Give the position of every leukocyte visible.
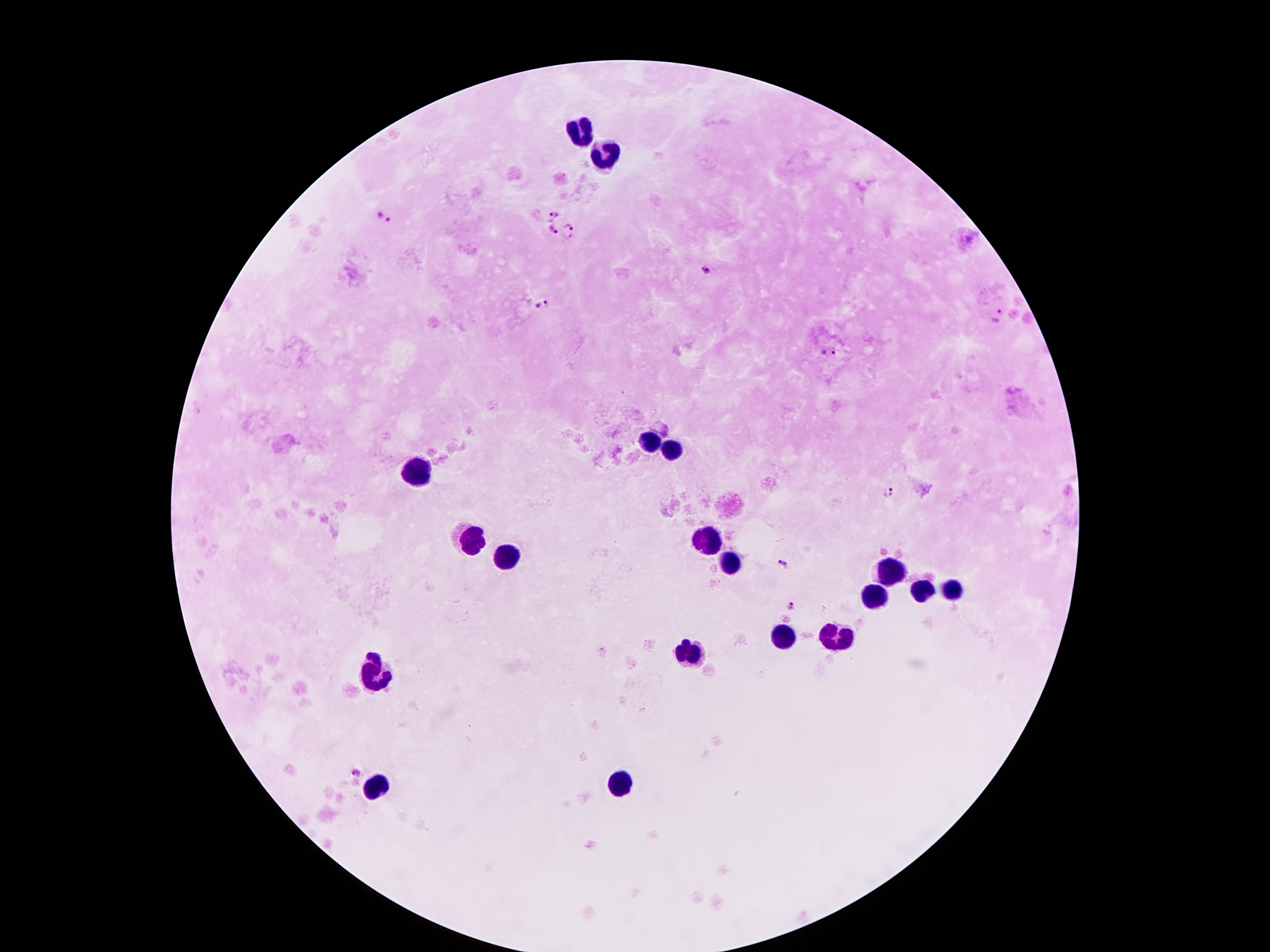
Approximate object centers, in pixels from the top-left corner.
Leukocytes: (x=584, y=133), (x=607, y=157), (x=651, y=440), (x=672, y=454), (x=418, y=475), (x=471, y=540), (x=706, y=540), (x=507, y=557), (x=729, y=566), (x=889, y=569), (x=924, y=592), (x=952, y=593), (x=874, y=599), (x=840, y=635), (x=782, y=637), (x=693, y=652), (x=376, y=675), (x=620, y=786), (x=377, y=790).

patient_malaria_status: infected with Plasmodium falciparum
preparation: thick peripheral-blood smear
field_of_view: one from this slide
malaria_parasite_locations: 'approximate object centers, in pixels from the top-left corner: (x=552, y=212), (x=384, y=218), (x=552, y=229), (x=568, y=229), (x=705, y=271), (x=543, y=305), (x=999, y=316), (x=827, y=353), (x=889, y=492), (x=784, y=562), (x=791, y=604), (x=357, y=775)'
capture: smartphone through the microscope eyepiece
magnification: 100x
stain: Giemsa
image_size: 1270×952 pixels